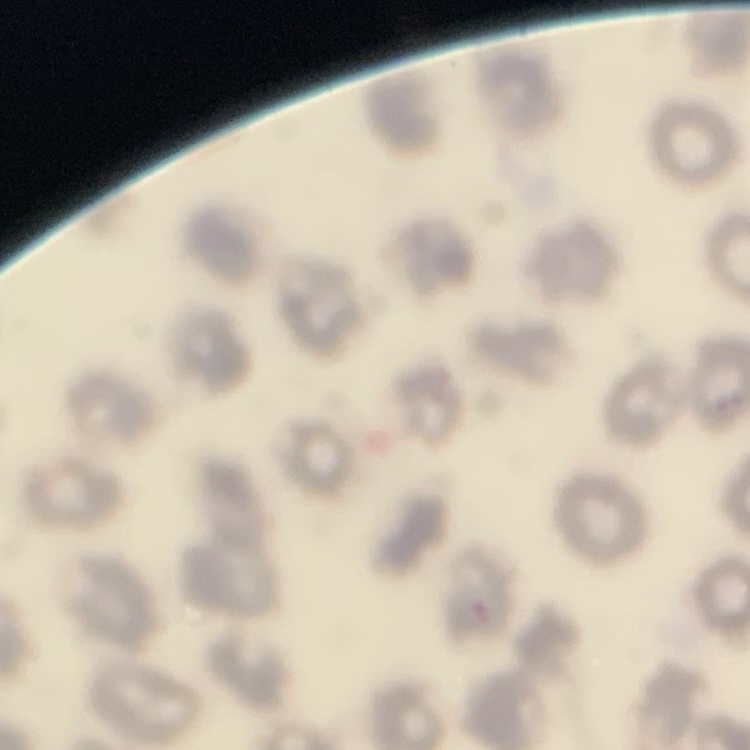 The erythrocytes show no rouleaux formation. Thin peripheral smear. Field's or Giemsa stain. Square crop of a larger photomicrograph.